Locate every blood parasite and identify its species.
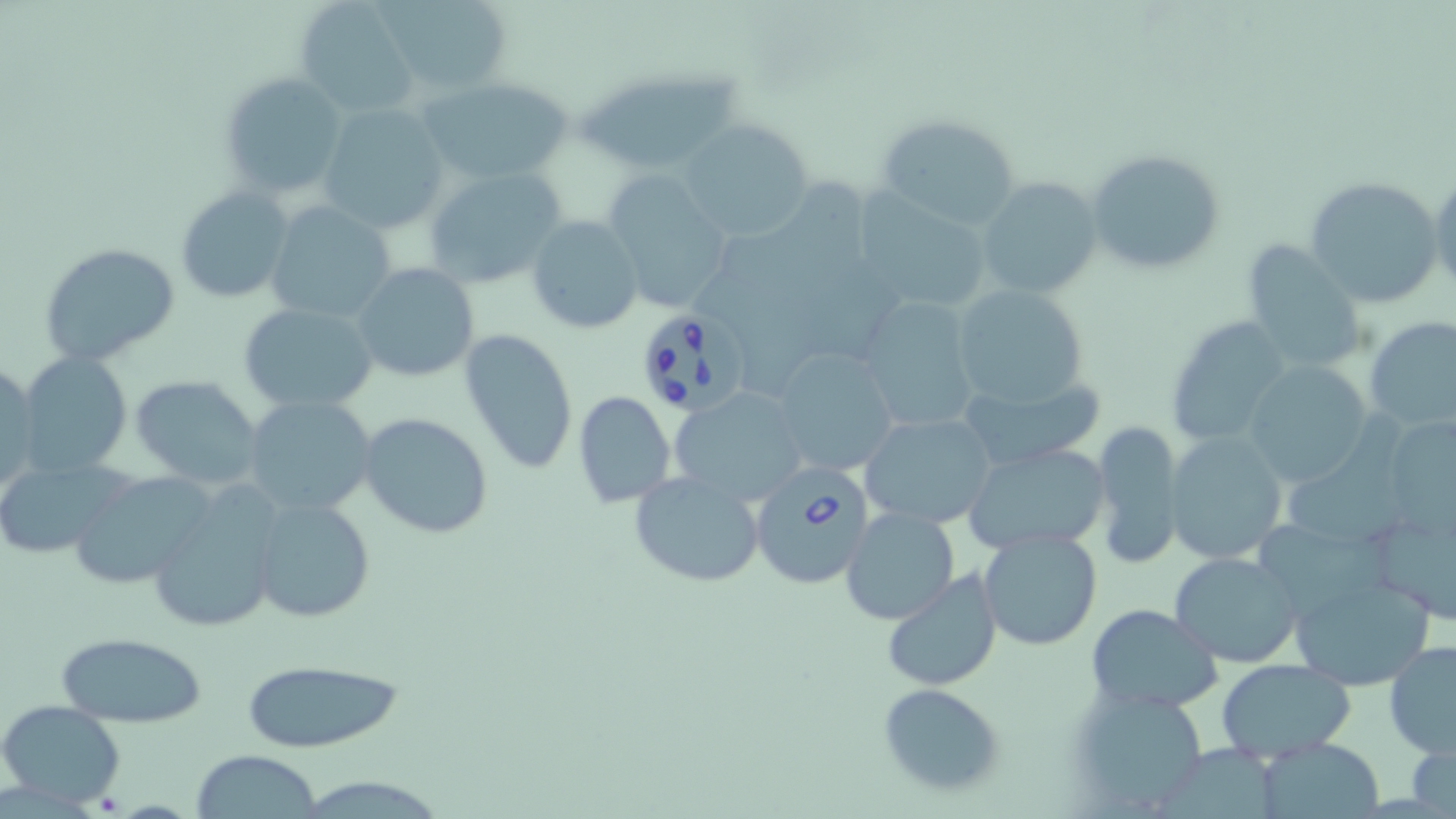
Approximate bounding boxes as named x1/y1/x2/y2 corners in pixels.
Babesia divergens-infected red blood cells: (x1=641, y1=307, x2=752, y2=419), (x1=749, y1=463, x2=875, y2=589).
No Plasmodium falciparum, Plasmodium ovale, Plasmodium malariae, Plasmodium vivax, or Trypanosoma brucei observed.

slide-level diagnosis = Babesia divergens
uninfected red blood cell locations = approximate bounding boxes as named x1/y1/x2/y2 corners in pixels: (x1=294, y1=0, x2=418, y2=118), (x1=377, y1=0, x2=513, y2=96), (x1=579, y1=70, x2=742, y2=174), (x1=219, y1=72, x2=348, y2=200), (x1=418, y1=76, x2=575, y2=187), (x1=320, y1=103, x2=449, y2=233), (x1=874, y1=112, x2=1027, y2=230), (x1=679, y1=117, x2=814, y2=240), (x1=1084, y1=148, x2=1224, y2=276), (x1=423, y1=165, x2=569, y2=291), (x1=1427, y1=169, x2=1455, y2=301), (x1=603, y1=171, x2=735, y2=313), (x1=1304, y1=174, x2=1445, y2=308), (x1=976, y1=177, x2=1102, y2=301), (x1=176, y1=186, x2=293, y2=303), (x1=864, y1=186, x2=990, y2=308), (x1=266, y1=202, x2=397, y2=322), (x1=527, y1=216, x2=642, y2=333), (x1=38, y1=241, x2=182, y2=367), (x1=1241, y1=241, x2=1365, y2=373), (x1=352, y1=263, x2=480, y2=383), (x1=951, y1=284, x2=1093, y2=411), (x1=857, y1=297, x2=981, y2=436), (x1=239, y1=302, x2=377, y2=415), (x1=1164, y1=317, x2=1292, y2=445), (x1=1364, y1=317, x2=1456, y2=433), (x1=460, y1=328, x2=578, y2=475), (x1=774, y1=345, x2=899, y2=475), (x1=16, y1=352, x2=133, y2=477), (x1=0, y1=361, x2=39, y2=496), (x1=1243, y1=363, x2=1370, y2=487), (x1=133, y1=376, x2=264, y2=488), (x1=968, y1=378, x2=1112, y2=467), (x1=670, y1=386, x2=810, y2=509), (x1=573, y1=392, x2=675, y2=508), (x1=244, y1=395, x2=378, y2=520), (x1=1281, y1=411, x2=1411, y2=554), (x1=358, y1=412, x2=494, y2=539), (x1=860, y1=412, x2=998, y2=527), (x1=1397, y1=416, x2=1456, y2=547), (x1=1093, y1=420, x2=1183, y2=570), (x1=1164, y1=432, x2=1287, y2=564), (x1=964, y1=442, x2=1110, y2=555), (x1=0, y1=456, x2=122, y2=557), (x1=628, y1=470, x2=767, y2=588), (x1=68, y1=471, x2=217, y2=589), (x1=146, y1=494, x2=280, y2=634), (x1=250, y1=496, x2=375, y2=623), (x1=842, y1=507, x2=959, y2=624), (x1=1258, y1=515, x2=1394, y2=612), (x1=1377, y1=520, x2=1456, y2=629), (x1=979, y1=527, x2=1103, y2=651), (x1=1169, y1=550, x2=1303, y2=669), (x1=880, y1=568, x2=1003, y2=693), (x1=1288, y1=569, x2=1438, y2=692), (x1=1087, y1=604, x2=1221, y2=714), (x1=56, y1=631, x2=208, y2=728), (x1=1383, y1=640, x2=1456, y2=758), (x1=241, y1=658, x2=406, y2=753), (x1=1214, y1=658, x2=1356, y2=763), (x1=1068, y1=683, x2=1211, y2=813), (x1=877, y1=684, x2=1005, y2=798), (x1=0, y1=700, x2=126, y2=805), (x1=1253, y1=737, x2=1387, y2=819), (x1=1409, y1=737, x2=1456, y2=819), (x1=1163, y1=742, x2=1277, y2=819), (x1=191, y1=750, x2=322, y2=819)
modality = optical microscopy
image size = 1456×819 pixels
magnification = 1000x
stain = May-Grünwald-Giemsa
preparation = thin blood film
field of view = single